Locate every uninfected red blood cell.
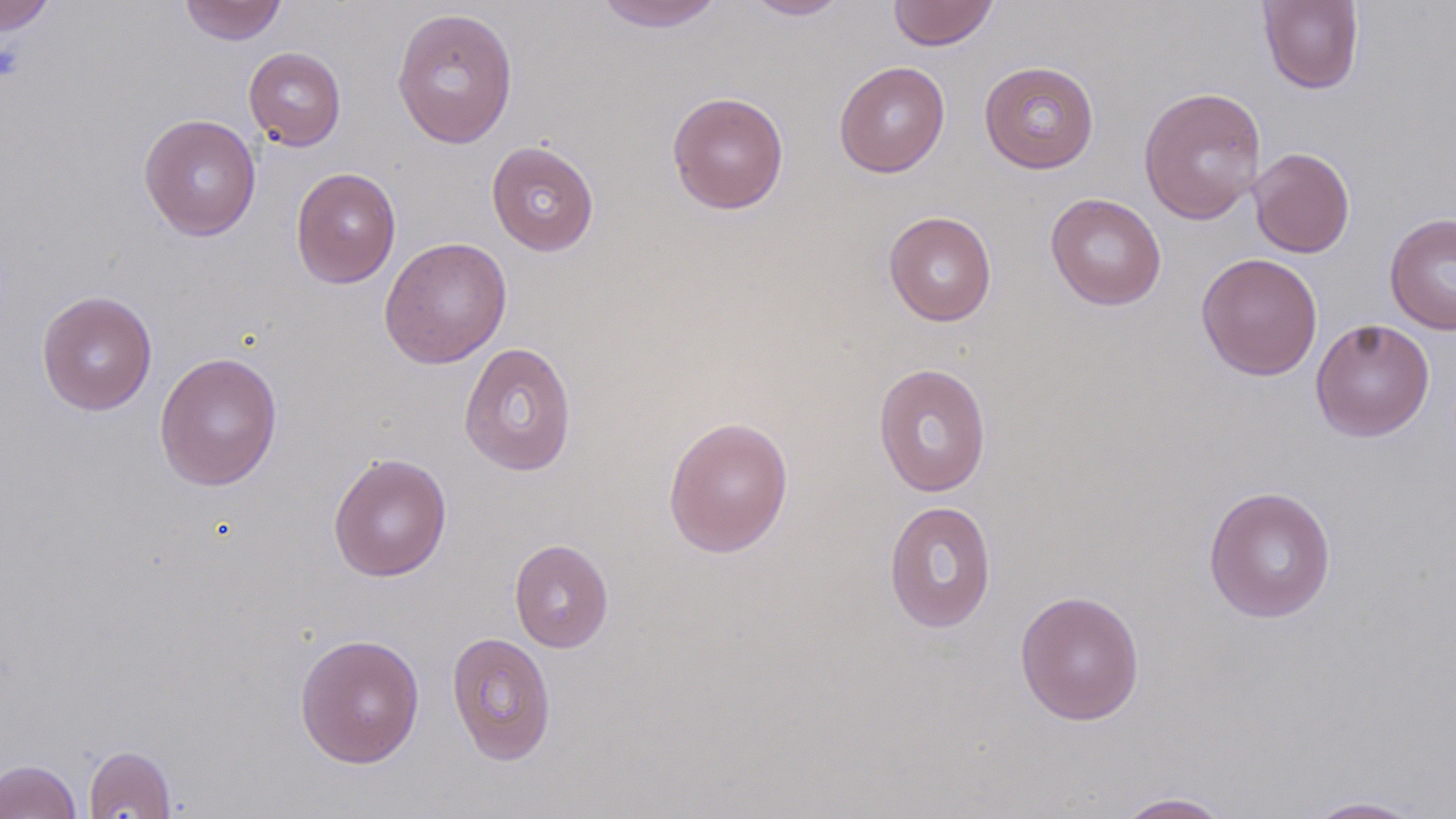

Approximate bounding boxes as named x1/y1/x2/y2 corners in pixels.
Uninfected red blood cells: (x1=179, y1=0, x2=288, y2=45), (x1=591, y1=0, x2=727, y2=32), (x1=742, y1=0, x2=853, y2=20), (x1=887, y1=0, x2=999, y2=50), (x1=0, y1=1, x2=56, y2=34), (x1=1257, y1=1, x2=1365, y2=94), (x1=391, y1=7, x2=519, y2=149), (x1=243, y1=46, x2=346, y2=151), (x1=834, y1=60, x2=951, y2=177), (x1=979, y1=61, x2=1099, y2=174), (x1=1138, y1=86, x2=1267, y2=224), (x1=667, y1=91, x2=789, y2=215), (x1=139, y1=113, x2=262, y2=241), (x1=486, y1=140, x2=600, y2=256), (x1=1249, y1=147, x2=1355, y2=258), (x1=291, y1=167, x2=401, y2=288), (x1=1045, y1=193, x2=1166, y2=310), (x1=883, y1=211, x2=997, y2=326), (x1=1384, y1=212, x2=1456, y2=335), (x1=379, y1=236, x2=512, y2=369), (x1=1195, y1=253, x2=1323, y2=381), (x1=37, y1=290, x2=157, y2=416), (x1=1310, y1=319, x2=1436, y2=441), (x1=458, y1=342, x2=578, y2=476), (x1=154, y1=352, x2=283, y2=491), (x1=873, y1=363, x2=992, y2=497), (x1=663, y1=416, x2=794, y2=557), (x1=328, y1=452, x2=452, y2=582), (x1=1203, y1=485, x2=1337, y2=623), (x1=883, y1=500, x2=997, y2=633), (x1=509, y1=539, x2=614, y2=653), (x1=1015, y1=589, x2=1145, y2=726), (x1=446, y1=631, x2=556, y2=766), (x1=294, y1=633, x2=425, y2=769), (x1=84, y1=745, x2=177, y2=818), (x1=0, y1=759, x2=82, y2=819), (x1=1112, y1=791, x2=1236, y2=818), (x1=1303, y1=796, x2=1432, y2=818).

Platelet locations: (x1=0, y1=41, x2=25, y2=83). Slide-level diagnosis: no evidence of blood parasites. May-Grünwald-Giemsa stain. Captured at 1000x magnification. Image is 1456×819 pixels. Thin blood smear. One field of a larger specimen. Optical microscopy.